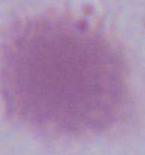
Summary:
  - Modality: micrograph
  - Magnification: 1000x
  - Identification: erythrocyte